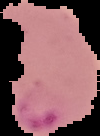 The area outside the segmented cell region is set to black. Result: Plasmodium parasites identified. Image is 100×136 pixels. From a thin blood smear.